Point out every malaria parasite.
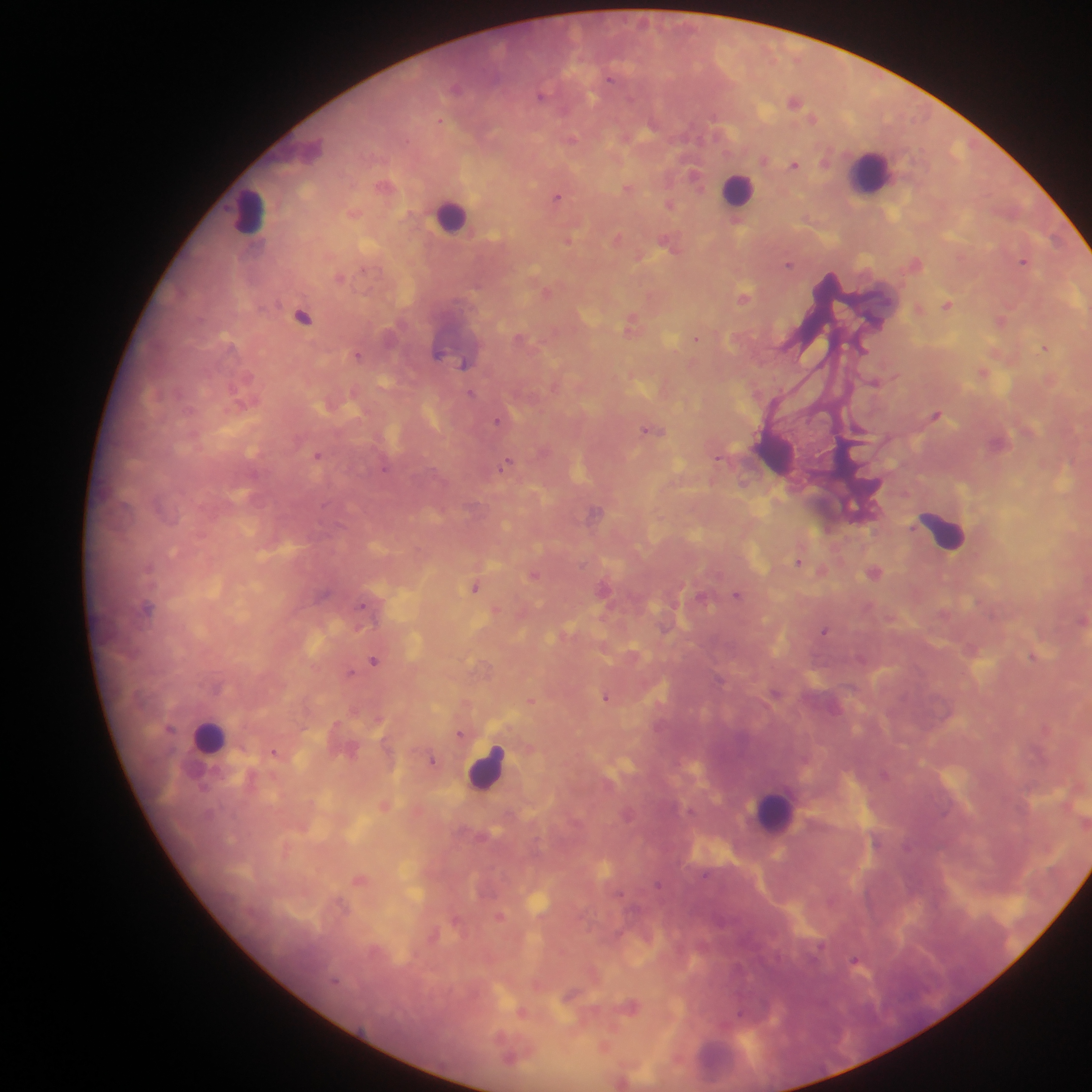
Approximate centers as {x, y} in pixels.
Malaria parasites: {795, 101}, {813, 120}, {795, 164}, {694, 178}, {558, 196}, {671, 203}, {618, 237}, {568, 240}, {1022, 261}, {789, 263}, {339, 276}, {745, 297}, {948, 306}, {632, 321}, {1003, 321}, {878, 324}, {698, 337}, {1045, 348}, {862, 349}, {442, 351}, {999, 354}, {463, 363}, {983, 373}, {248, 376}, {895, 376}, {877, 384}, {231, 386}, {472, 392}, {937, 414}, {498, 420}, {650, 430}, {319, 455}, {719, 458}, {499, 468}, {173, 555}, {798, 563}, {150, 568}, {535, 575}, {475, 587}, {737, 594}, {362, 604}, {496, 608}, {361, 626}, {824, 630}, {1032, 656}, {374, 660}, {352, 672}, {606, 697}, {531, 700}, {1047, 729}, {460, 734}, {275, 751}, {434, 759}, {884, 774}, {286, 851}, {660, 883}, {500, 916}, {458, 918}, {856, 959}, {632, 1005}, {741, 1012}, {606, 1046}.

Leukocyte locations: {868, 169}, {739, 193}, {249, 208}, {453, 217}, {945, 532}, {205, 737}, {487, 768}, {773, 815}. Collected in Ghana. Image is 1092×1092 pixels. Mobile-phone photograph taken through the microscope. One field of view. Thick blood smear.